Give the position of every Plasmodium parasite.
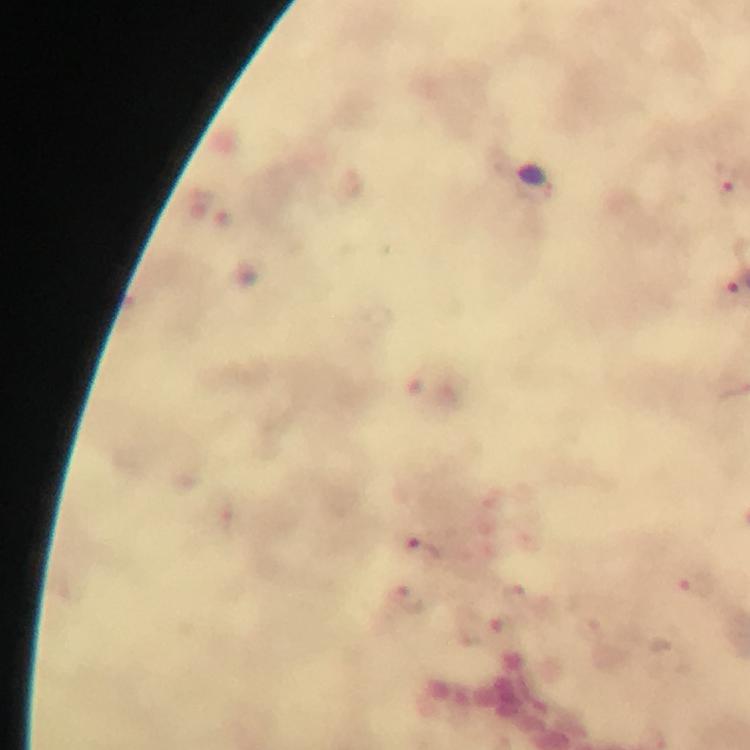
Approximate object centers, in pixels from the top-left corner.
Plasmodium parasites: (x=725, y=181), (x=423, y=549), (x=699, y=583), (x=515, y=592), (x=408, y=599).

Giemsa-stained preparation. Image is 750×750 pixels. At 100x magnification. A crop from one field of view. Photographed with a smartphone mounted on the microscope. Immersion oil applied. Thick blood smear. From a diagnostic examination for malaria.